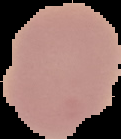

The area outside the segmented cell region is set to black. From a thin blood film. Image is 121×139 pixels. Malaria status: uninfected.